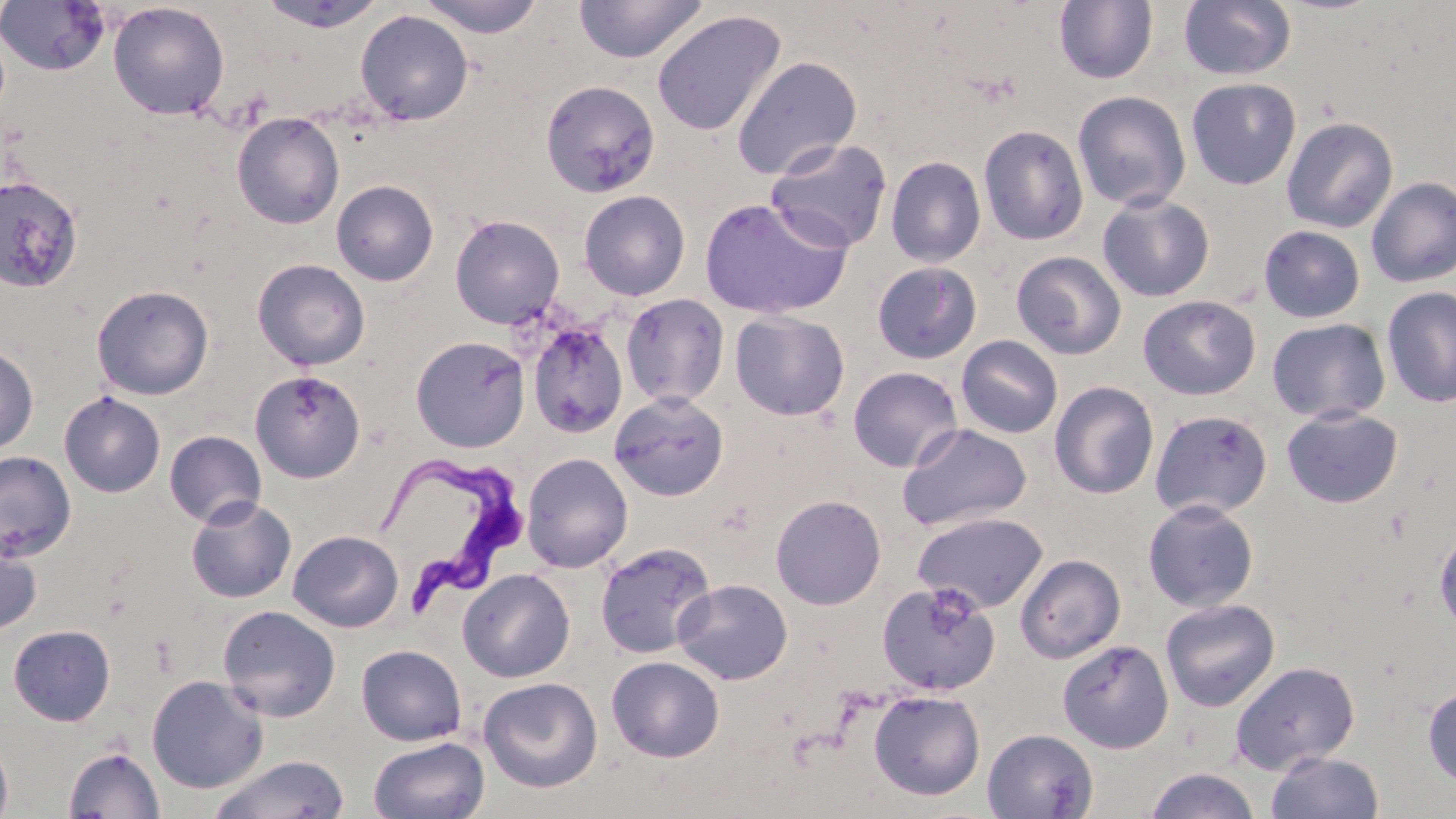
Approximate bounding boxes as (x1, y1, x2, y2) in pixels. Trypanosoma brucei locations: (379, 454, 532, 620). Uninfected red blood cell locations: (417, 0, 547, 39), (574, 0, 708, 64), (0, 1, 109, 76), (258, 1, 388, 33), (1053, 1, 1158, 85), (1178, 1, 1296, 81), (107, 2, 230, 120), (651, 9, 786, 137), (355, 10, 474, 126), (732, 55, 862, 180), (1186, 78, 1301, 190), (539, 79, 660, 198), (1072, 90, 1191, 211), (231, 111, 345, 230), (1281, 116, 1399, 233), (978, 123, 1089, 246), (765, 137, 893, 253), (885, 156, 986, 267), (0, 175, 83, 293), (1366, 176, 1456, 287), (331, 180, 439, 286), (578, 189, 691, 301), (1098, 193, 1215, 303), (699, 195, 852, 319), (449, 214, 564, 328), (1258, 225, 1365, 323), (1011, 251, 1126, 360), (253, 259, 370, 371), (872, 261, 982, 364), (91, 284, 214, 400), (1381, 286, 1456, 409), (620, 292, 730, 408), (1138, 295, 1260, 401), (730, 311, 850, 420), (526, 318, 628, 439), (1266, 318, 1390, 423), (956, 335, 1063, 439), (410, 336, 529, 452), (0, 344, 38, 455), (847, 366, 963, 473), (250, 369, 366, 483), (1049, 381, 1159, 499), (59, 391, 165, 497), (609, 391, 729, 501), (1281, 406, 1403, 508), (1150, 409, 1272, 521), (896, 422, 1032, 533), (164, 430, 267, 527), (0, 451, 77, 562), (521, 452, 633, 572), (770, 493, 887, 610), (185, 496, 297, 603), (1142, 499, 1259, 612), (911, 513, 1048, 613), (287, 530, 404, 632), (1434, 530, 1456, 635), (0, 532, 42, 637), (595, 541, 717, 659), (1015, 553, 1126, 663), (457, 568, 575, 683), (673, 578, 793, 685), (876, 581, 1000, 696), (1160, 598, 1281, 713), (217, 604, 341, 722), (7, 624, 115, 726), (1056, 639, 1174, 753), (356, 643, 468, 746), (606, 656, 725, 762), (1229, 660, 1361, 775), (145, 674, 268, 794), (478, 677, 603, 792), (1422, 684, 1456, 787), (867, 690, 985, 801), (982, 728, 1099, 819), (0, 735, 13, 819), (368, 735, 490, 819), (63, 745, 166, 819), (1266, 750, 1386, 819), (208, 754, 351, 819), (1144, 768, 1261, 818). Slide-level diagnosis: Trypanosoma brucei. Thin blood film. Image is 1456×819 pixels. One field of a larger specimen. 1000x magnification. May-Grünwald-Giemsa-stained preparation. Optical microscopy.